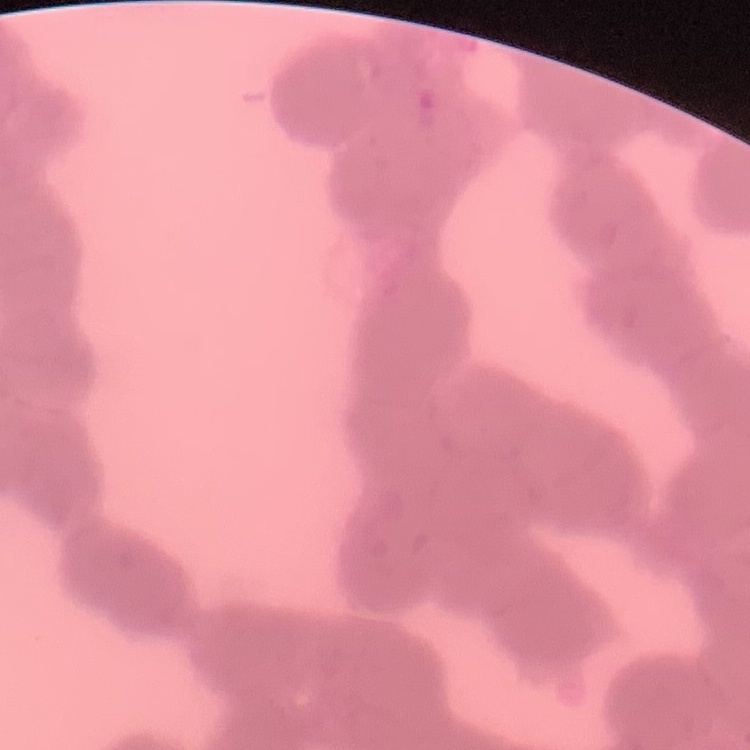
red blood cell morphology = rouleaux formation
preparation = thin blood smear
stain = Field's or Giemsa
image type = one tile cut from a larger photomicrograph